Identify the cell.
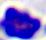

A leukocyte.

Captured at 400x magnification. Micrograph.